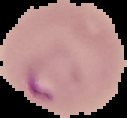
From a thin blood film. Image is 127×118 pixels. Segmented cell region on a black background. Malaria status: parasitized.